Classify this cell by malaria status.
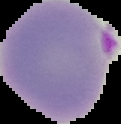
It is parasitized.

Image is 121×124 pixels. Cell region segmented out of the field of view; the surrounding area is masked to black. From a thin blood smear.